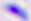
Captured at 400x magnification. Toxoplasma gondii is seen. Photomicrograph.